Comment on the morphology of the erythrocytes.
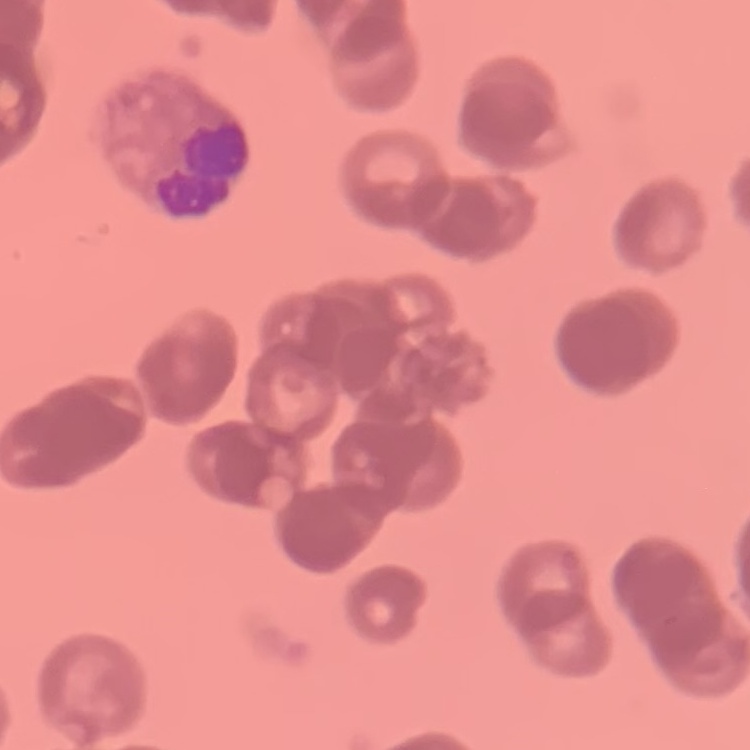
Rouleaux formation.

image type = square crop of a larger photomicrograph
stain = Field's or Giemsa
preparation = thin blood film